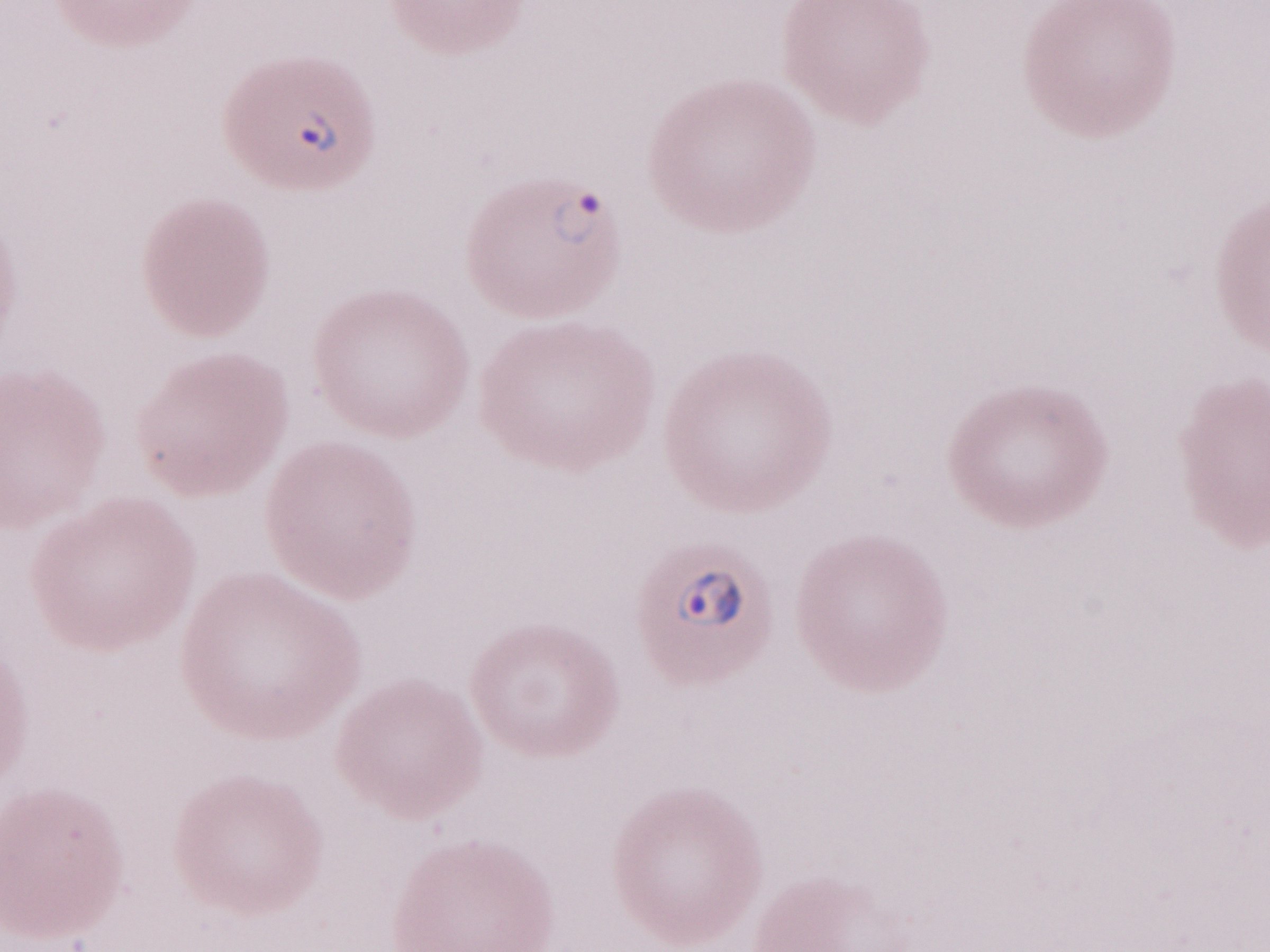

Thin blood smear. Olympus BX43 microscope, Olympus DP73 camera. Patient diagnosis: malaria infection. One field of this slide. May-Grünwald-Giemsa stain. Magnification: 1,000x. Image is 1270×952 pixels.